Assess the morphology of the erythrocytes.
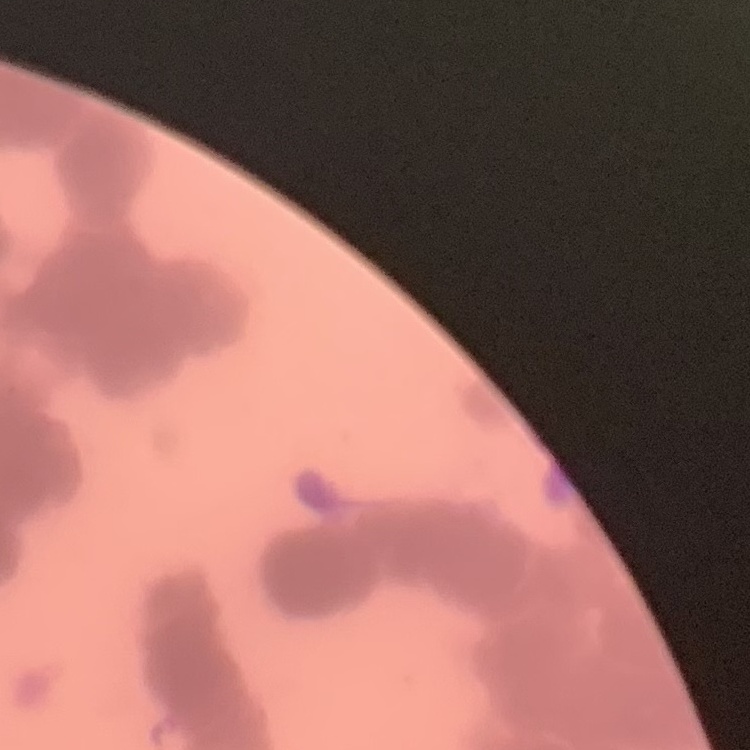

They show rouleaux formation.

Summary:
  - Image type: square crop of a larger photomicrograph
  - Stain: Field's or Giemsa
  - Preparation: thin blood film